Identify the parasite.
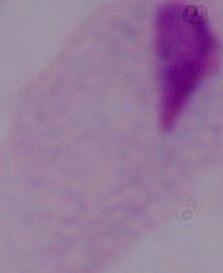

A trichomonad.

Photomicrograph. Captured at 1000x magnification.